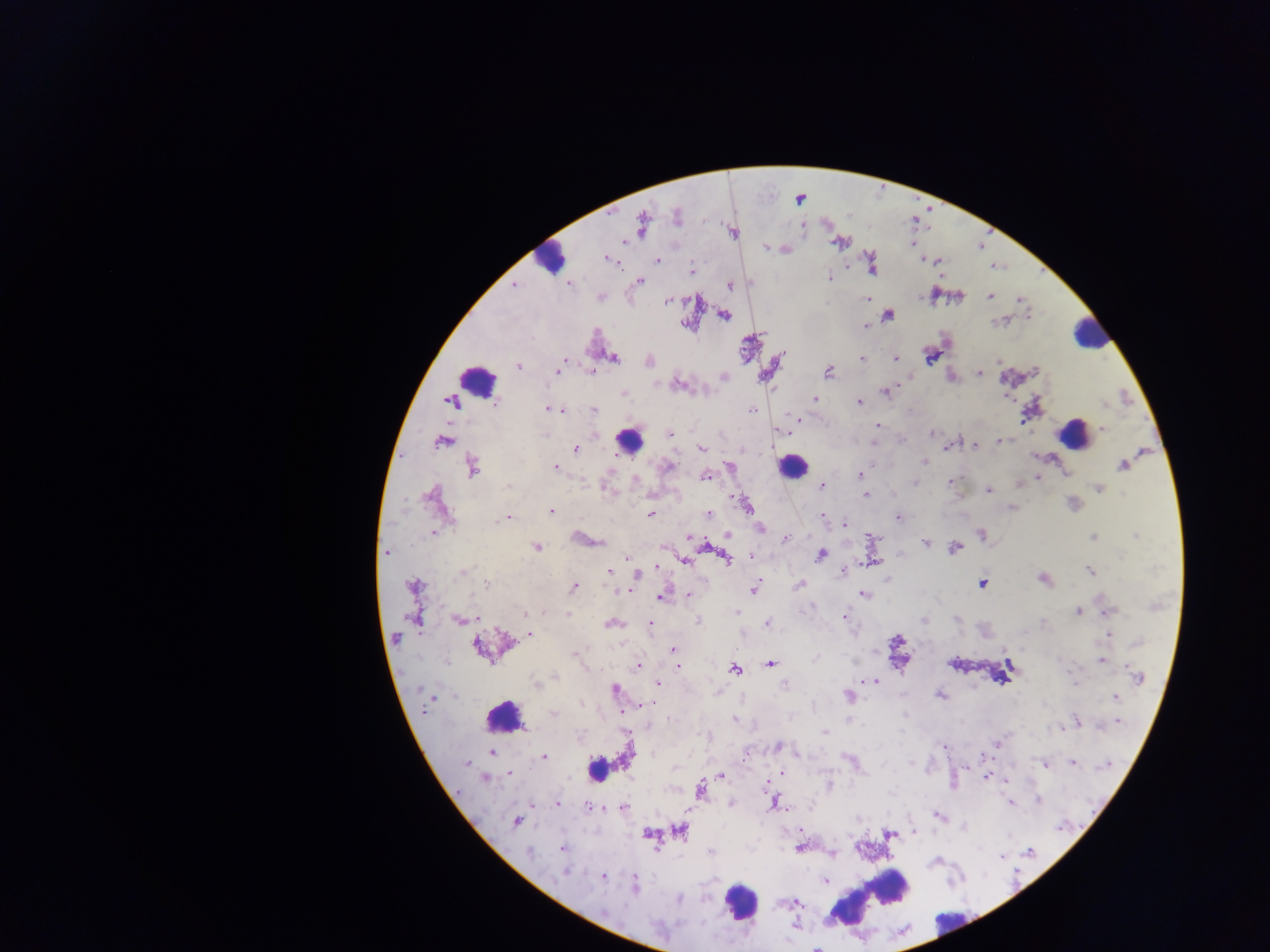

Approximate centers as [x, y] in pixels.
Summary:
  - Plasmodium parasite locations: [677, 217], [642, 222], [837, 242], [766, 248], [607, 259], [657, 260], [923, 260], [939, 261], [691, 271], [829, 278], [640, 281], [569, 284], [514, 285], [729, 286], [990, 296], [600, 298], [1020, 299], [867, 300], [666, 301], [888, 315], [724, 316], [996, 322], [684, 324], [866, 326], [614, 357], [930, 357], [861, 359], [895, 359], [999, 361], [518, 366], [561, 366], [558, 370], [591, 372], [829, 372], [1035, 372], [979, 373], [678, 385], [885, 392], [623, 394], [815, 398], [496, 403], [859, 403], [1103, 404], [548, 410], [594, 410], [751, 411], [562, 412], [795, 419], [877, 425], [1103, 429], [932, 433], [669, 434], [999, 441], [440, 443], [874, 443], [975, 445], [948, 446], [701, 447], [576, 449], [925, 461], [1123, 465], [472, 467], [555, 467], [667, 467], [731, 467], [860, 475], [707, 476], [1038, 478], [636, 479], [950, 481], [915, 483], [1020, 484], [509, 485], [823, 486], [1099, 489], [989, 490], [429, 495], [865, 495], [745, 504], [1012, 507], [551, 511], [652, 513], [707, 514], [823, 516], [507, 517], [898, 518], [502, 519], [845, 523], [760, 527], [433, 533], [981, 534], [728, 535], [1135, 536], [688, 537], [1093, 537], [785, 539], [599, 541], [925, 542], [704, 544], [537, 546], [954, 548], [386, 553], [821, 555], [751, 556], [626, 557], [727, 559], [685, 560], [657, 567], [843, 570], [1090, 571], [462, 572], [609, 572], [637, 575], [1043, 580], [982, 583], [486, 585], [800, 585], [414, 587], [574, 587], [755, 588], [618, 592], [689, 594], [863, 594], [661, 597], [1109, 610], [543, 612], [736, 612], [1078, 612], [525, 613], [567, 613], [844, 617], [956, 619], [459, 620], [923, 620], [697, 621], [767, 623], [1043, 623], [610, 624], [650, 625], [530, 634], [1108, 635], [395, 638], [1137, 642], [478, 647], [673, 650], [576, 653], [1100, 660], [770, 664], [637, 666], [678, 666], [734, 670], [1138, 676], [554, 677], [875, 681], [1074, 681], [535, 684], [658, 684], [784, 684], [614, 689], [940, 695], [848, 696], [1116, 697], [582, 704], [648, 704], [553, 714], [669, 719], [735, 719], [1077, 721], [1118, 722], [1100, 726], [1060, 729], [825, 732], [997, 743], [944, 746], [778, 747], [491, 752], [983, 755], [627, 756], [544, 758], [466, 762], [1072, 763], [1044, 764], [1107, 765], [509, 773], [782, 773], [721, 776], [987, 776], [484, 778], [1006, 780], [766, 783], [828, 784], [701, 789], [1038, 800], [774, 803], [557, 804], [730, 804], [1011, 804], [588, 806], [624, 808], [938, 816], [517, 822], [964, 827], [680, 832], [647, 834], [889, 835], [799, 847], [563, 848], [711, 851], [1029, 851], [530, 852], [832, 855], [1002, 857], [565, 873], [604, 877], [825, 881], [635, 887], [678, 898], [604, 912]
  - Leukocyte locations: [549, 258], [1089, 335], [476, 379], [1073, 435], [627, 441], [792, 466], [503, 717], [596, 769], [870, 898], [740, 901], [950, 923]
  - Capture: mobile-phone photograph through a microscope
  - Image size: 1270×952 pixels
  - Preparation: thick blood film
  - Country: Ghana
  - Field of view: single